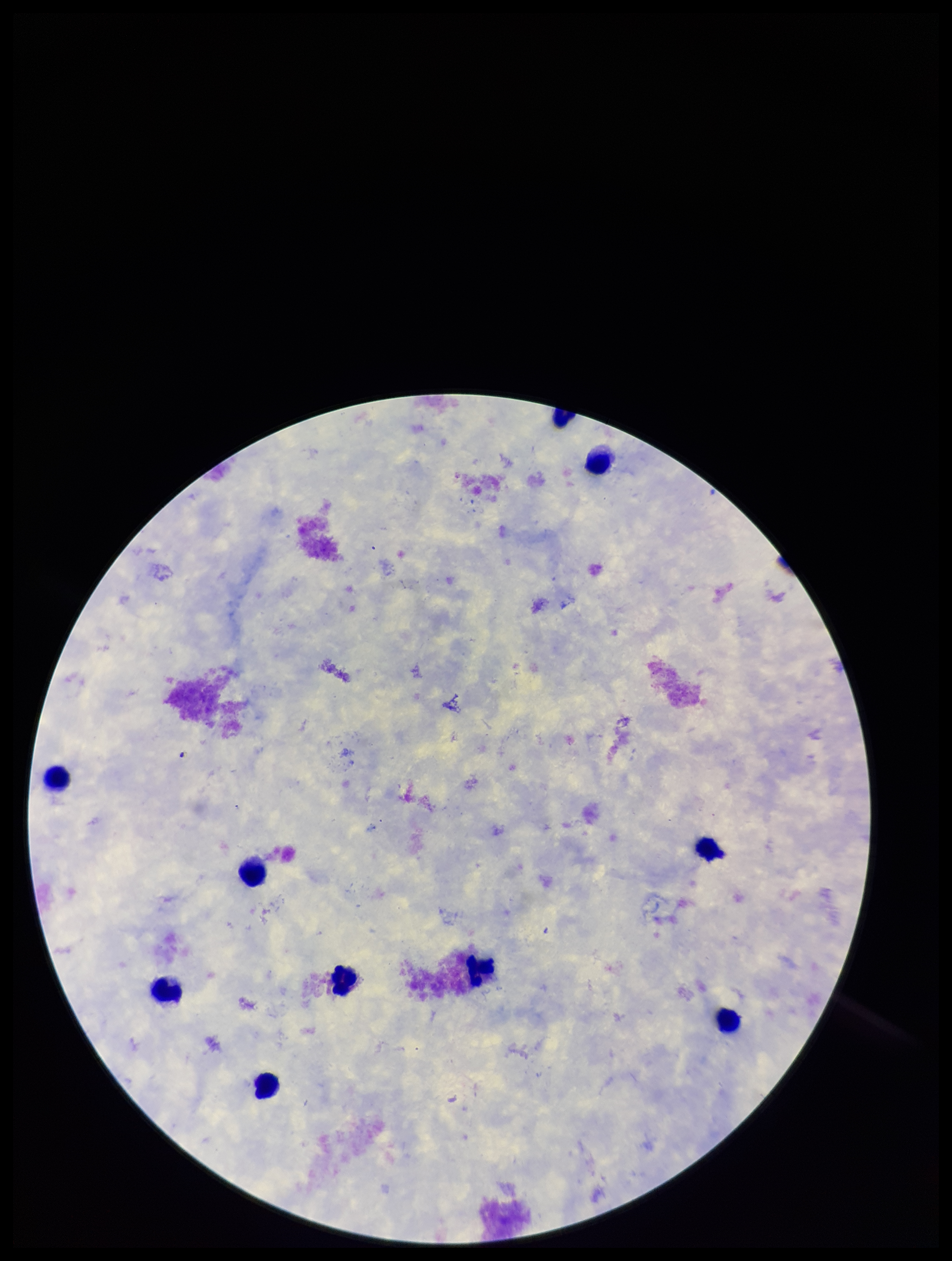
Summary:
  - Leukocyte count: 10
  - Stain: Giemsa
  - Patient malaria status: negative
  - Preparation: thick blood smear
  - Parasite count: 0
  - Field of view: one from this slide
  - Image size: 952×1261 pixels
  - Plasmodium parasites: none seen
  - Capture: smartphone photograph through the microscope eyepiece